Give the extent of all Plasmodium falciparum-infected red blood cells.
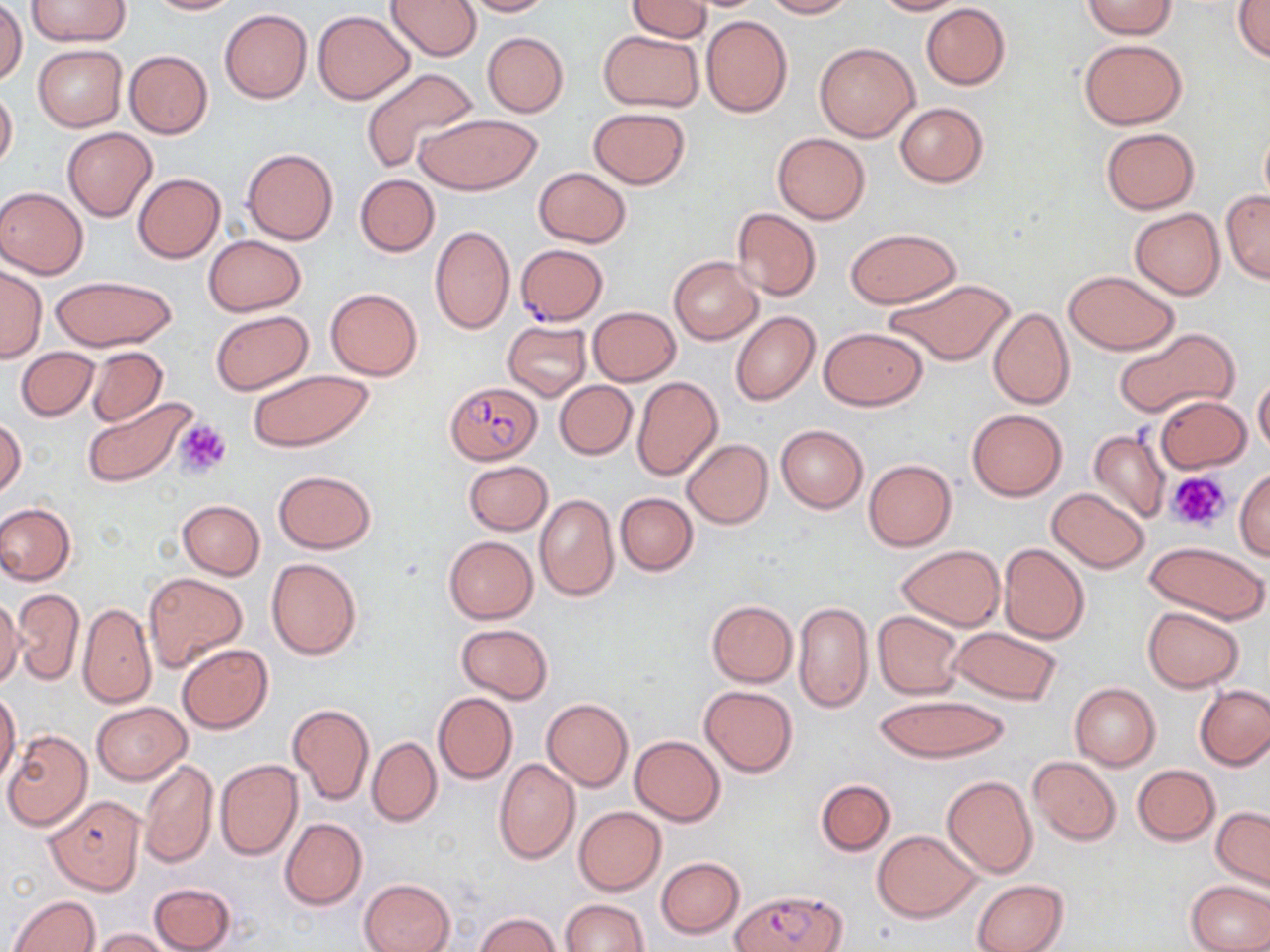
Approximate bounding boxes as (x1,y1)-(x2,y2) corner pairs in pixels.
Plasmodium falciparum-infected red blood cells: (516,248)-(611,329), (445,381)-(542,466), (44,798)-(145,898), (733,890)-(846,952).

Uninfected red blood cell locations: (28,0)-(131,46), (146,0)-(240,15), (387,0)-(482,60), (455,0)-(554,16), (624,0)-(712,41), (760,0)-(854,18), (870,0)-(964,16), (1081,1)-(1178,38), (1231,2)-(1270,62), (0,3)-(26,84), (921,3)-(1011,90), (219,8)-(312,104), (312,10)-(415,104), (702,15)-(792,117), (599,29)-(704,112), (481,31)-(569,117), (1077,39)-(1187,129), (814,41)-(919,141), (33,44)-(127,132), (124,51)-(213,137), (359,66)-(476,174), (0,86)-(18,171), (895,102)-(988,187), (588,107)-(691,189), (413,113)-(542,194), (1259,122)-(1270,211), (63,127)-(157,220), (1100,128)-(1200,213), (772,132)-(871,224), (241,147)-(339,245), (533,167)-(632,248), (133,173)-(225,264), (355,174)-(439,257), (0,187)-(87,279), (1221,189)-(1270,284), (731,207)-(821,300), (1130,207)-(1225,299), (430,225)-(515,334), (846,228)-(961,309), (203,235)-(306,316), (669,256)-(763,344), (0,264)-(45,363), (1063,270)-(1178,355), (50,275)-(178,351), (881,277)-(1016,365), (325,288)-(423,381), (587,306)-(681,386), (988,306)-(1075,410), (211,309)-(312,395), (731,311)-(819,406), (502,320)-(592,400), (1113,326)-(1239,420), (819,327)-(929,410), (87,346)-(167,427), (16,347)-(99,421), (244,369)-(374,452), (631,376)-(724,481), (1252,376)-(1270,458), (554,380)-(638,459), (1155,395)-(1250,473), (82,398)-(195,487), (968,409)-(1067,501), (1,417)-(25,498), (775,425)-(867,513), (1087,429)-(1169,523), (681,438)-(773,529), (863,460)-(956,551), (463,461)-(553,535), (1160,464)-(1245,541), (273,469)-(376,553), (1235,469)-(1270,560), (1047,487)-(1151,572), (615,492)-(698,575), (534,493)-(618,602), (176,499)-(265,578), (0,502)-(76,585), (443,535)-(538,623), (1143,541)-(1269,623), (998,543)-(1091,645), (896,545)-(1005,631), (266,557)-(362,659), (143,572)-(247,673), (12,588)-(85,685), (0,597)-(24,690), (706,600)-(798,687), (794,601)-(872,714), (78,602)-(155,707), (1142,607)-(1244,692), (872,612)-(966,699), (455,624)-(553,703), (948,627)-(1062,704), (177,644)-(273,733), (1069,683)-(1160,770), (1196,684)-(1270,770), (699,685)-(797,776), (0,689)-(21,786), (433,691)-(517,785), (873,695)-(1012,763), (542,698)-(633,790), (92,701)-(192,784), (287,703)-(374,805), (2,730)-(92,831), (630,736)-(725,825), (367,737)-(442,825), (1028,756)-(1121,844), (215,759)-(303,861), (493,759)-(581,865), (140,760)-(218,868), (1133,765)-(1219,845), (942,775)-(1038,880), (815,779)-(895,855), (573,806)-(666,895), (1211,806)-(1270,891), (279,817)-(367,911), (872,831)-(981,922), (656,857)-(744,938), (359,878)-(455,952), (973,879)-(1069,952), (1186,880)-(1270,951), (149,881)-(237,952), (8,894)-(102,952), (559,899)-(650,952), (475,912)-(560,952), (90,928)-(173,951). Platelet locations: (173,416)-(231,480), (1167,470)-(1232,533). Slide-level diagnosis: Plasmodium falciparum. Captured at 1000x magnification. Optical microscopy. Image is 1270×952 pixels. May-Grünwald-Giemsa stain. Single field of view. Thin blood film.